Locate every blood parasite and identify its species.
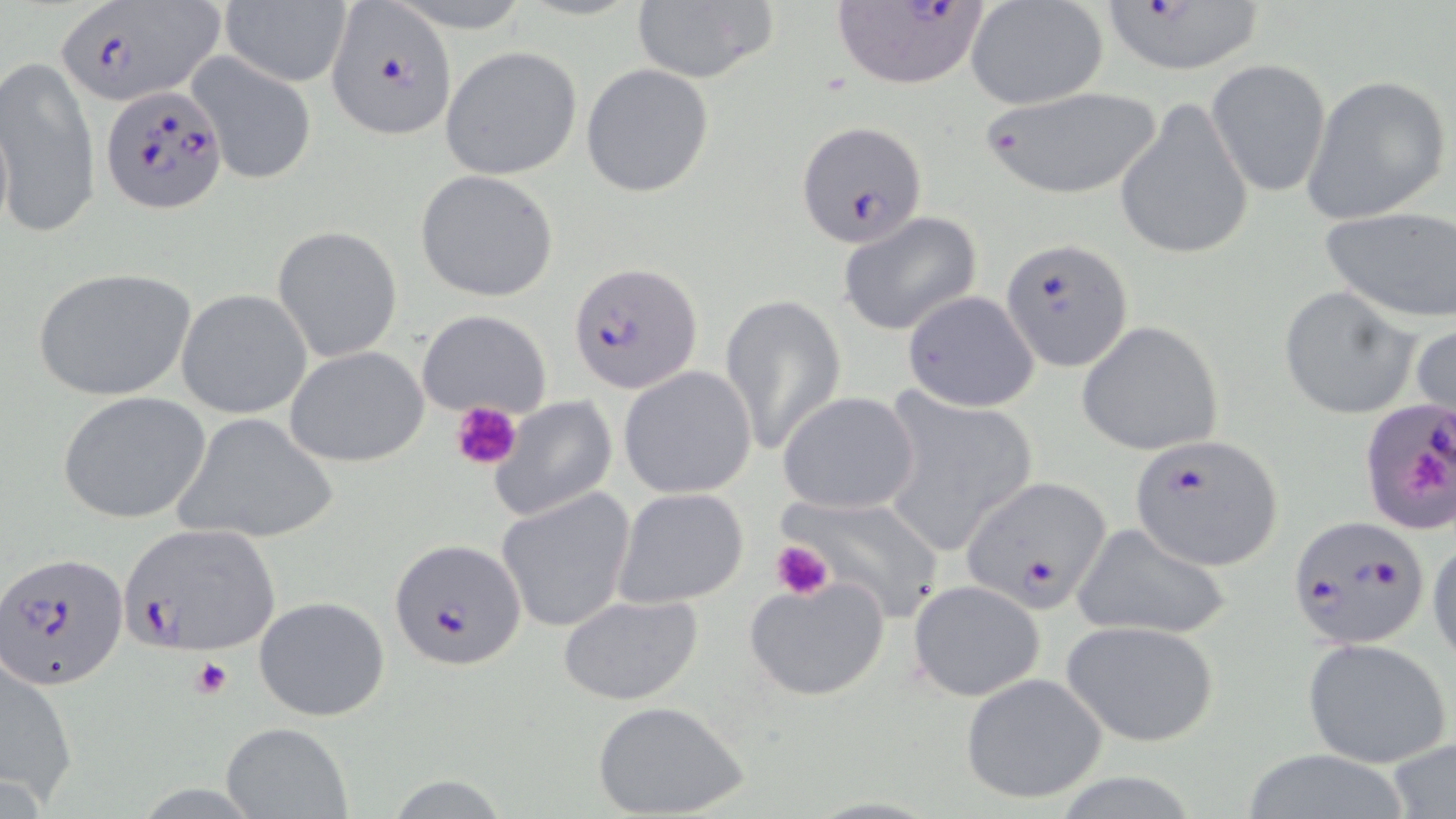
Approximate bounding boxes as (x1,y1)-(x2,y2) corner pairs in pixels.
Plasmodium falciparum-infected red blood cells: (52,1)-(221,106), (323,1)-(457,141), (1098,1)-(1268,76), (831,3)-(991,90), (99,83)-(228,213), (797,122)-(926,246), (1001,239)-(1133,372), (570,264)-(703,394), (1360,397)-(1456,537), (1130,433)-(1285,570), (960,477)-(1112,614), (1288,514)-(1431,650), (121,524)-(282,655), (390,539)-(526,669), (0,552)-(126,691).
No Plasmodium ovale, Plasmodium malariae, Plasmodium vivax, Babesia divergens, or Trypanosoma brucei observed.

Uninfected red blood cell locations: (217,0)-(352,88), (629,1)-(775,85), (966,1)-(1110,110), (439,45)-(583,180), (184,51)-(318,187), (0,57)-(99,240), (1207,60)-(1331,198), (581,65)-(714,197), (1301,74)-(1452,224), (975,87)-(1167,200), (1115,97)-(1254,260), (0,106)-(15,244), (414,169)-(559,303), (1319,207)-(1456,324), (836,210)-(987,337), (273,226)-(403,361), (32,266)-(197,402), (1278,287)-(1417,421), (176,289)-(312,419), (901,290)-(1041,413), (721,291)-(846,457), (415,309)-(551,420), (1078,321)-(1223,457), (1410,321)-(1455,427), (284,346)-(429,468), (617,366)-(757,499), (875,388)-(1040,559), (776,390)-(922,515), (58,392)-(209,524), (488,396)-(619,523), (173,414)-(337,543), (613,487)-(749,609), (497,489)-(635,633), (772,491)-(950,618), (1071,521)-(1232,641), (1427,536)-(1456,668), (742,574)-(892,702), (908,580)-(1045,701), (556,593)-(704,706), (253,595)-(390,721), (1062,620)-(1219,746), (1302,637)-(1452,769), (1,651)-(80,808), (959,672)-(1110,806), (593,700)-(750,818), (218,721)-(353,819), (1387,737)-(1456,817), (385,776)-(511,816). Platelet locations: (451,400)-(521,470), (1412,454)-(1451,499), (770,539)-(832,600), (190,657)-(234,700). Slide-level diagnosis: Plasmodium falciparum. Single field of view. May-Grünwald-Giemsa stain. Light microscopy. 1000x magnification. Image is 1456×819 pixels. Thin blood film.